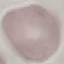

Result: negative for malaria parasites. Giemsa-stained preparation. Thin smear of blood. Automatically extracted cell patch, resized to 64 × 64 pixels. Photographed with a smartphone camera at the microscope eyepiece.